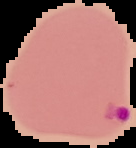
Summary:
  - Malaria status: parasitized
  - Preparation: thin blood smear
  - Image type: cell region segmented out of the field of view; surrounding area masked to black
  - Image size: 136×148 pixels